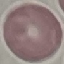
Summary:
  - Malaria status: uninfected
  - Capture: smartphone through the microscope eyepiece
  - Preparation: thin smear
  - Stain: Giemsa
  - Image type: cell patch, automatically extracted from a larger field of view and resized to 64 × 64 pixels